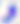

Captured at 400x magnification. Micrograph. Toxoplasma gondii is shown.